Name the parasite shown.
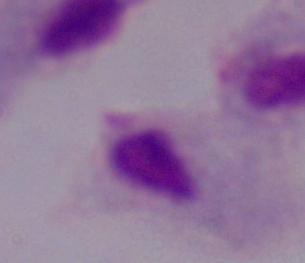

A trichomonad.

modality = photomicrograph
magnification = 1000x